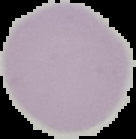

Segmented cell region on a black background. Malaria status: uninfected. Image is 136×139 pixels. From a thin blood film.